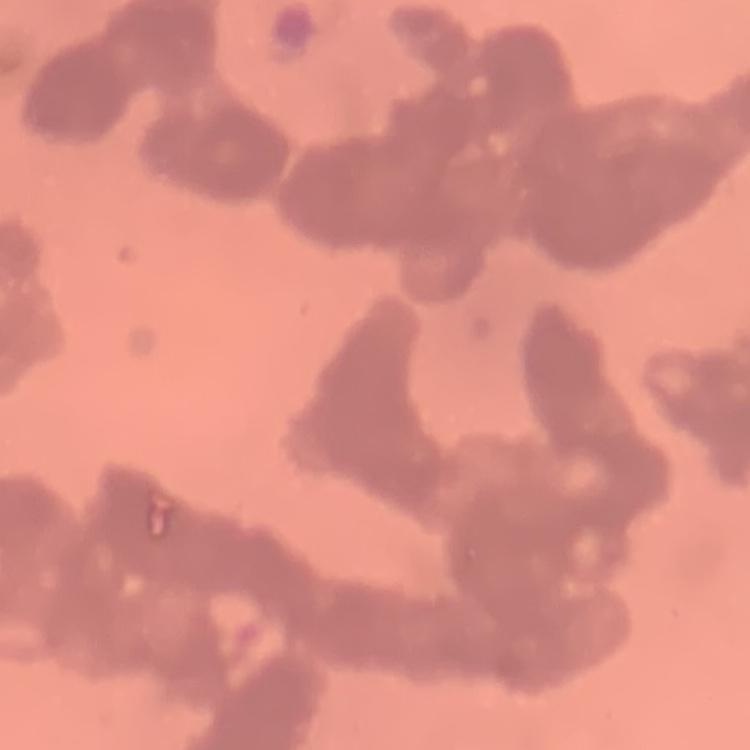

Summary:
  - Erythrocyte morphology: rouleaux formation
  - Image type: one tile cut from a larger photomicrograph
  - Stain: Field's or Giemsa
  - Preparation: thin blood smear